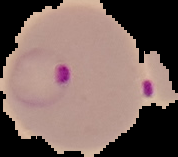

Summary:
  - Image type: segmented cell region on a black background
  - Preparation: thin blood film
  - Image size: 178×157 pixels
  - Result: Plasmodium parasites identified